Give the extent of all Plasmodium vivax-infected red blood cells.
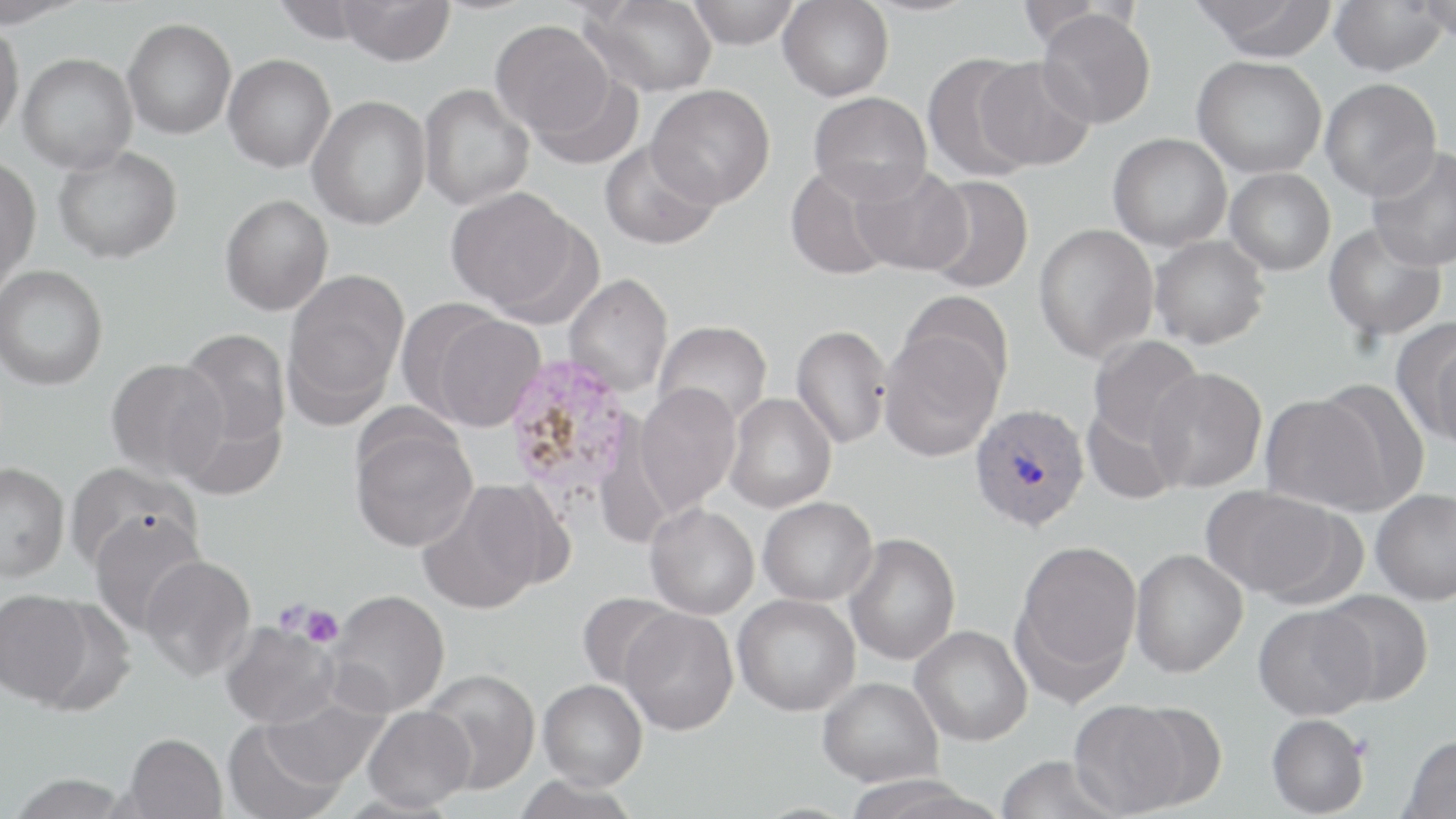

Approximate bounding boxes as [x1, y1, x2, y2] in pixels.
Plasmodium vivax-infected red blood cells: [501, 353, 640, 508], [969, 403, 1090, 531].

Uninfected red blood cell locations: [0, 0, 88, 28], [272, 0, 370, 43], [338, 0, 454, 65], [686, 0, 800, 49], [1329, 0, 1448, 76], [1415, 0, 1456, 43], [579, 1, 718, 97], [778, 1, 894, 101], [1192, 1, 1339, 61], [1036, 9, 1156, 128], [122, 17, 236, 139], [491, 18, 618, 141], [0, 23, 24, 143], [17, 53, 138, 174], [223, 54, 336, 172], [922, 54, 1037, 182], [1192, 56, 1327, 178], [975, 57, 1094, 171], [530, 71, 646, 170], [1320, 78, 1442, 201], [418, 83, 535, 210], [646, 84, 774, 209], [808, 91, 932, 202], [307, 95, 431, 230], [1108, 132, 1232, 251], [600, 139, 722, 249], [53, 146, 182, 264], [1366, 146, 1456, 271], [0, 157, 41, 289], [785, 162, 901, 281], [851, 165, 972, 276], [1225, 168, 1336, 275], [920, 175, 1034, 294], [445, 186, 582, 315], [220, 194, 333, 315], [1033, 223, 1159, 364], [1323, 223, 1446, 341], [1149, 236, 1269, 349], [0, 264, 108, 390], [281, 270, 408, 424], [563, 273, 673, 397], [897, 292, 1012, 402], [423, 309, 546, 432], [653, 320, 772, 428], [1394, 320, 1456, 445], [791, 324, 893, 449], [178, 328, 291, 451], [879, 328, 1004, 461], [1088, 335, 1205, 449], [1430, 338, 1456, 455], [106, 357, 228, 481], [1145, 367, 1267, 493], [1311, 378, 1431, 510], [635, 383, 741, 514], [173, 390, 288, 501], [724, 393, 837, 513], [1260, 393, 1387, 513], [1081, 404, 1183, 505], [349, 418, 479, 552], [0, 462, 70, 582], [65, 462, 200, 575], [418, 482, 550, 615], [1201, 486, 1342, 600], [1370, 488, 1456, 605], [758, 496, 877, 605], [645, 503, 759, 619], [87, 509, 207, 635], [844, 533, 960, 665], [1014, 539, 1142, 686], [1130, 548, 1248, 678], [139, 554, 256, 682], [0, 589, 93, 706], [326, 589, 451, 716], [1315, 589, 1435, 706], [577, 592, 682, 691], [732, 593, 860, 716], [1252, 604, 1378, 721], [619, 607, 739, 735], [221, 621, 339, 729], [910, 625, 1033, 746], [420, 668, 541, 794], [818, 676, 943, 787], [538, 678, 648, 790], [263, 693, 388, 790], [1068, 700, 1192, 817], [362, 705, 476, 811], [1266, 714, 1370, 817], [222, 719, 345, 819], [123, 732, 227, 819], [1401, 734, 1456, 818], [995, 755, 1124, 819], [7, 774, 134, 818], [511, 775, 640, 819], [840, 775, 999, 818]. Platelet locations: [297, 603, 343, 649]. Slide-level diagnosis: Plasmodium vivax. Captured at 1000x magnification. One field of a larger specimen. Optical microscopy. Thin blood smear. Image is 1456×819 pixels. May-Grünwald-Giemsa stain.